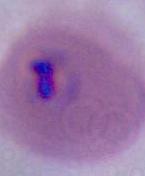 Micrograph. A Plasmodium parasite is seen. Captured at either 400x or 1000x magnification.